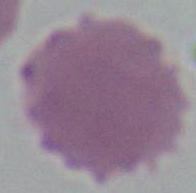

identification: red blood cell
magnification: 1000x
modality: photomicrograph